Report the malaria status of this cell.
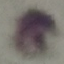
It is uninfected.

{
  "stain": "Giemsa",
  "preparation": "thin blood smear",
  "capture": "smartphone through the microscope eyepiece",
  "image_type": "cell patch, automatically extracted from a larger field of view and resized to 64 × 64 pixels"
}